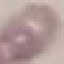
malaria status = uninfected
image type = cell patch, automatically extracted from a larger field of view and resized to 64 × 64 pixels
stain = Giemsa
capture = smartphone through the microscope eyepiece
preparation = thin blood smear